Comment on the morphology of the erythrocytes.
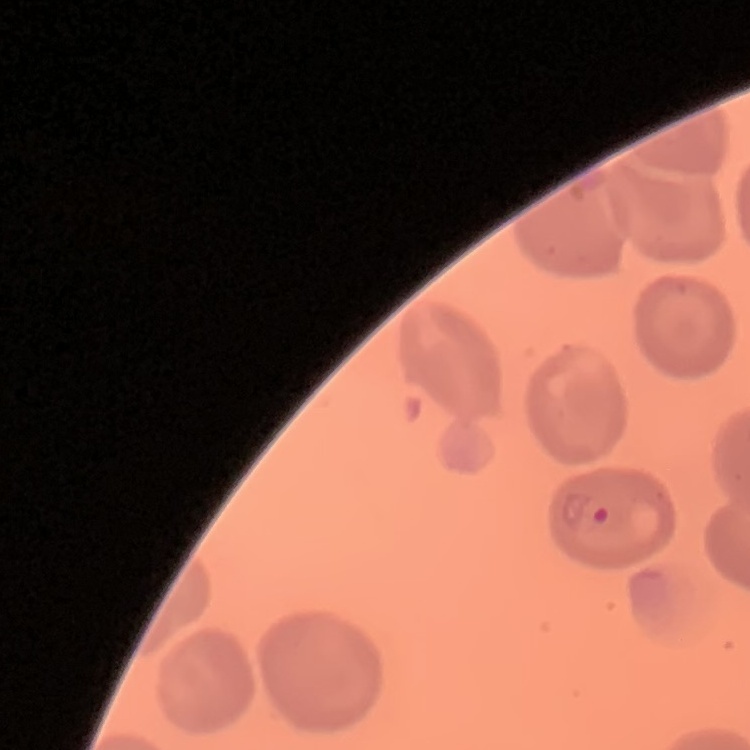
They show no rouleaux formation.

Field's or Giemsa stain. Thin peripheral smear. One tile cut from a larger photomicrograph.